Give the preparation type.
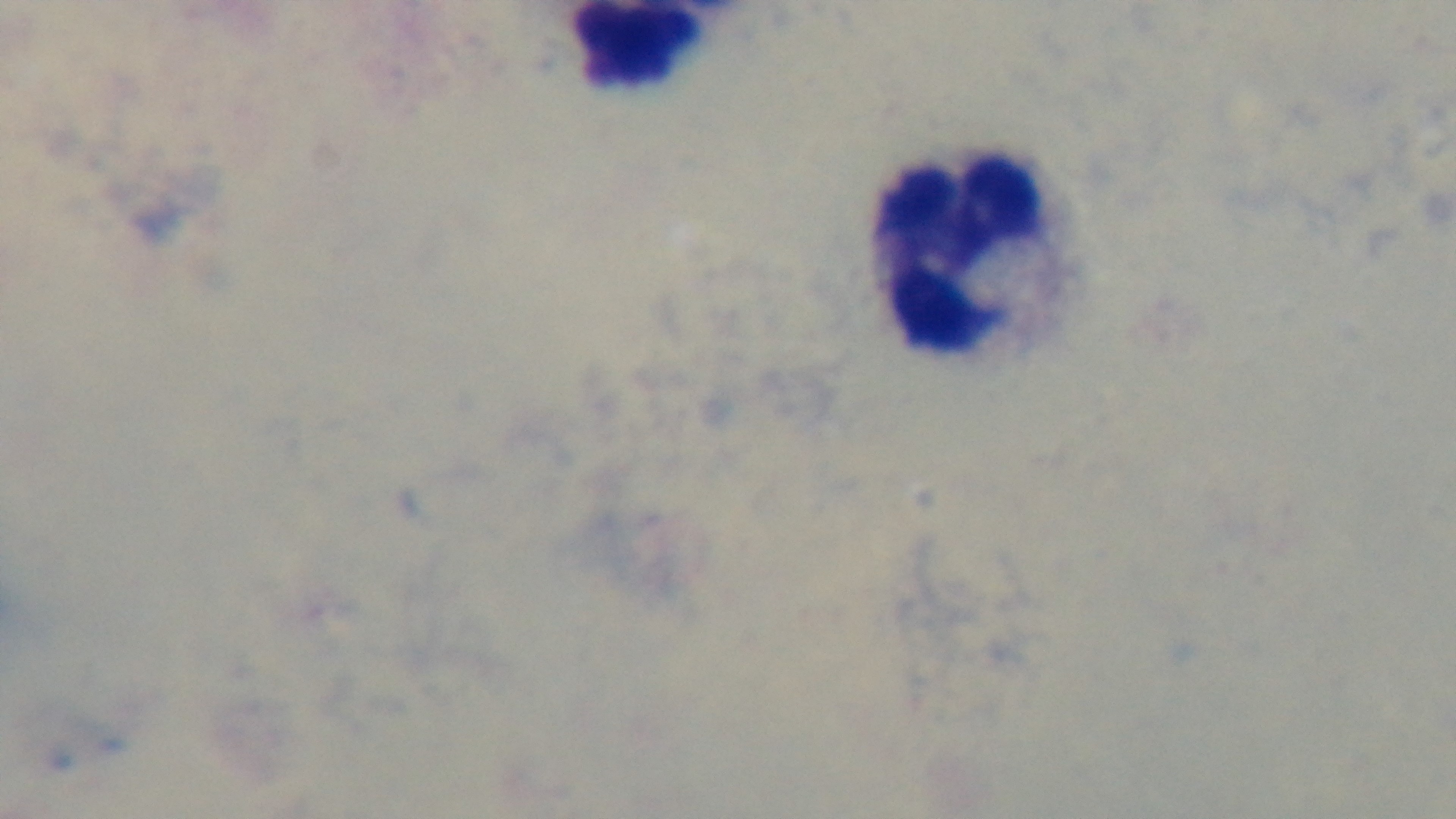

It is a thick blood film.

Summary:
  - Stain: Giemsa
  - Objective: 100x oil immersion
  - Field of view: one from the slide
  - Modality: light microscopy
  - Capture: mounted 4K digital camera
  - Malaria status: negative